Identify the parasite.
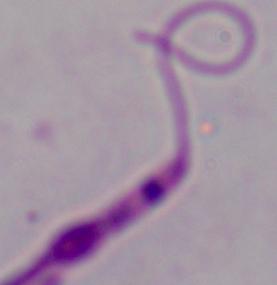
Leishmania.

magnification: 1000x
modality: micrograph